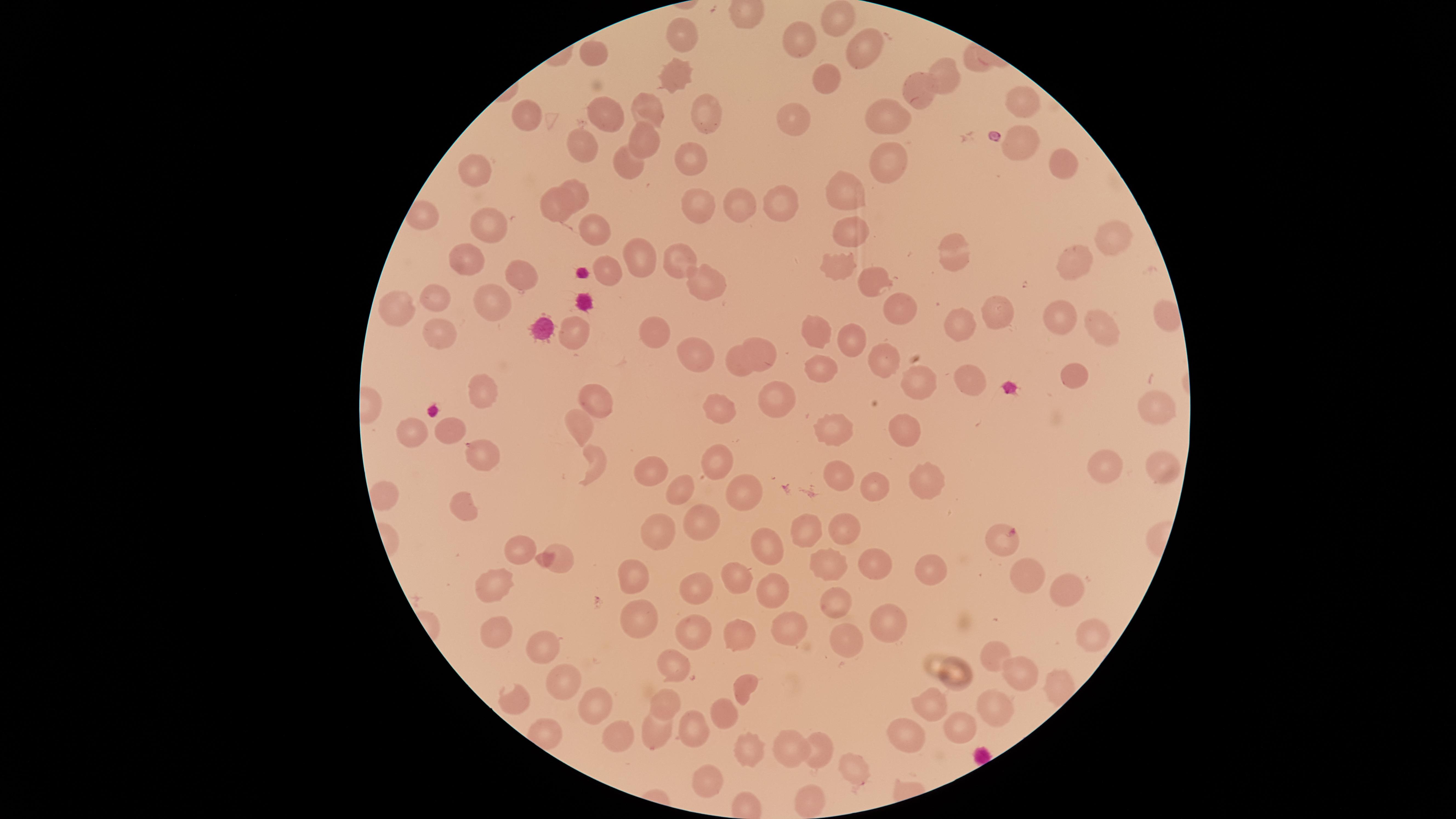
Approximate marker points as {x, y} in pixels. Uninfected RBCs: {841, 21}, {687, 38}, {799, 42}, {594, 54}, {856, 55}, {947, 73}, {679, 74}, {822, 88}, {917, 93}, {1021, 105}, {650, 106}, {529, 110}, {608, 113}, {700, 113}, {881, 116}, {793, 117}, {647, 138}, {1015, 144}, {585, 146}, {1060, 157}, {690, 159}, {887, 165}, {477, 167}, {628, 167}, {574, 188}, {847, 192}, {781, 196}, {731, 199}, {694, 203}, {554, 207}, {487, 224}, {849, 227}, {594, 233}, {1115, 240}, {953, 250}, {640, 256}, {465, 257}, {674, 260}, {841, 261}, {1076, 261}, {609, 270}, {519, 274}, {700, 276}, {870, 276}, {434, 299}, {492, 304}, {400, 308}, {992, 308}, {1166, 308}, {898, 310}, {1057, 314}, {958, 319}, {1096, 325}, {814, 331}, {653, 332}, {574, 334}, {443, 336}, {851, 336}, {765, 349}, {692, 353}, {887, 356}, {736, 365}, {825, 367}, {1073, 370}, {914, 378}, {976, 382}, {480, 390}, {774, 391}, {594, 397}, {1150, 400}, {716, 406}, {582, 422}, {906, 426}, {455, 428}, {832, 428}, {413, 433}, {479, 455}, {603, 457}, {715, 462}, {1106, 464}, {1161, 465}, {650, 468}, {838, 479}, {686, 485}, {880, 485}, {917, 485}, {740, 490}, {465, 505}, {696, 514}, {845, 529}, {654, 530}, {807, 530}, {764, 544}, {521, 545}, {563, 558}, {831, 560}, {878, 560}, {930, 566}, {633, 569}, {1035, 577}, {731, 581}, {697, 586}, {498, 587}, {1063, 587}, {775, 588}, {835, 599}, {637, 617}, {883, 622}, {499, 626}, {783, 626}, {1091, 634}, {841, 636}, {738, 638}, {693, 639}, {995, 653}, {540, 655}, {672, 666}, {957, 669}, {1013, 672}, {745, 683}, {557, 685}, {516, 696}, {593, 702}, {664, 702}, {932, 705}, {995, 705}, {726, 708}, {653, 727}, {693, 730}, {960, 730}, {621, 735}, {906, 735}, {749, 741}, {819, 748}, {792, 749}, {847, 765}, {708, 773}, {812, 800}. Parasitized RBCs: {1000, 535}. Circular visible region. Thin blood film. Photographed with a smartphone camera through the microscope eyepiece. Species: Plasmodium falciparum. Image is 1456×819 pixels. One field of view of the specimen. Giemsa-stained preparation. Presence: malaria parasites identified.